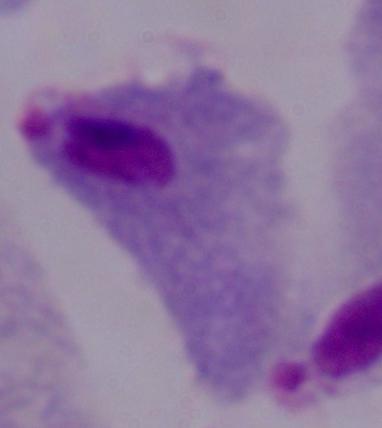

identification = trichomonad
magnification = 1000x
modality = micrograph